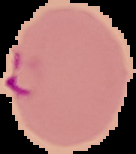
Summary:
  - Image type: cell region segmented out of the field of view; surrounding area masked to black
  - Result: malaria parasites detected
  - Image size: 136×154 pixels
  - Preparation: thin blood film